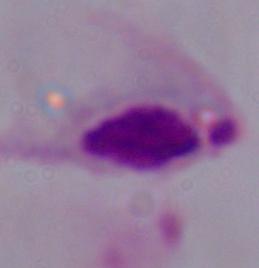
identification: trichomonad
magnification: 1000x
modality: photomicrograph